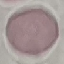
result: negative for malaria parasites
capture: smartphone camera at the microscope eyepiece
stain: Giemsa
image_type: cell patch, automatically extracted from a larger field of view and resized to 64 × 64 pixels
preparation: thin smear